Assess the morphology of the red blood cells.
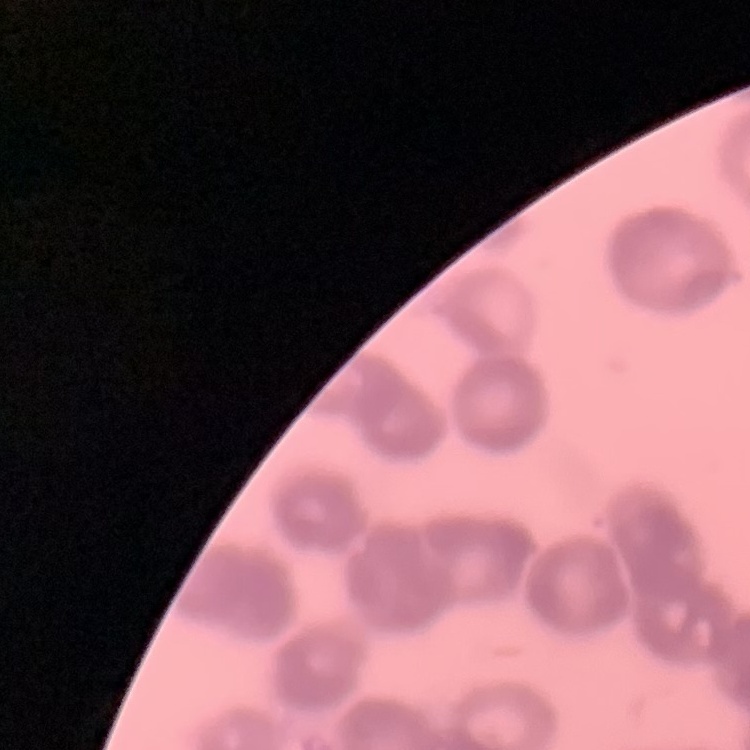
Rouleaux formation.

One tile cut from a larger photomicrograph. Thin blood smear. Field's or Giemsa stain.